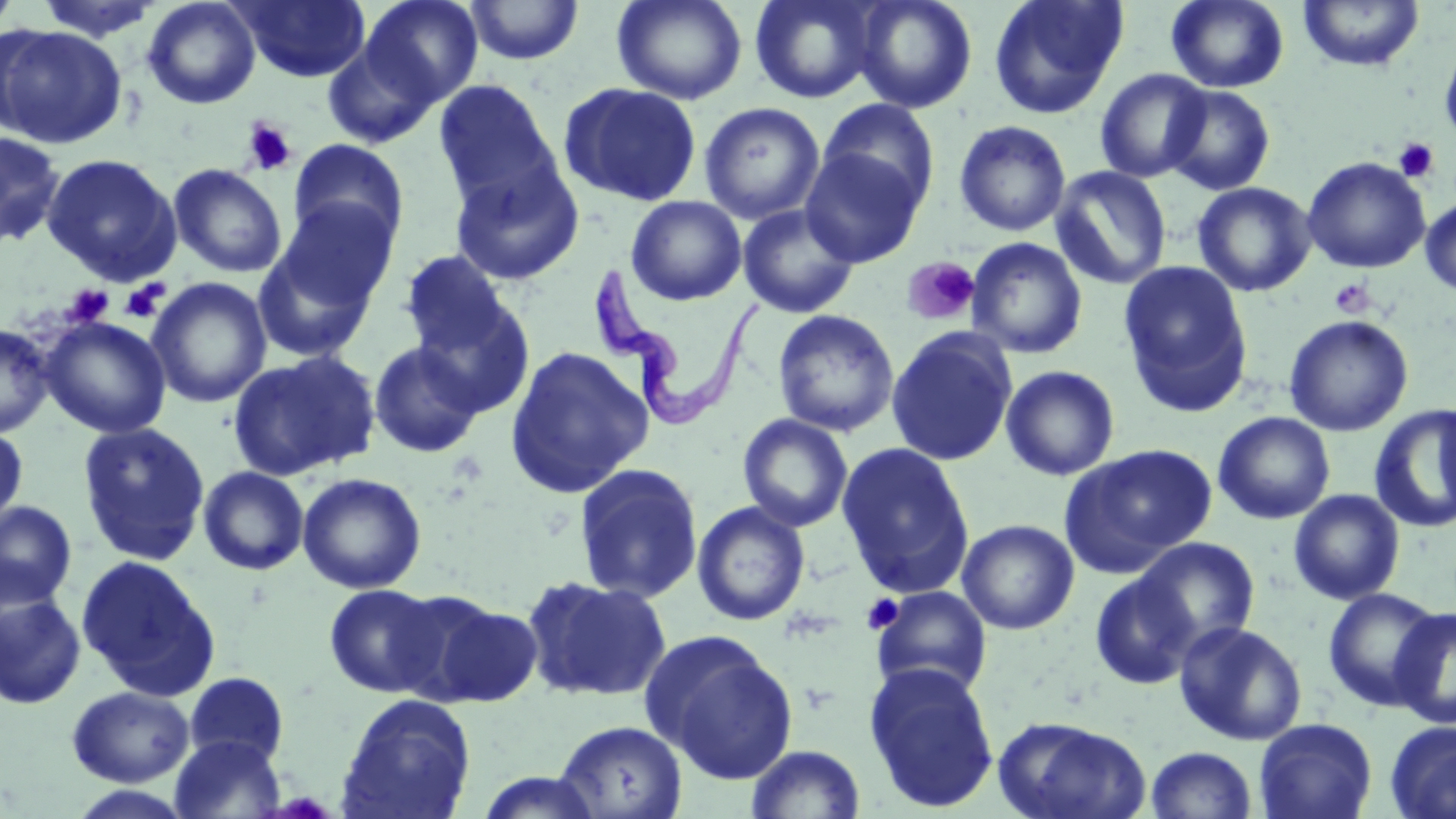 Approximate bounding boxes as (x1,y1)-(x2,y2) corner pairs in pixels. Platelet locations: (242,119)-(297,176), (1393,137)-(1438,183), (901,256)-(979,326), (1329,278)-(1376,319), (121,280)-(168,322), (65,285)-(114,327), (862,593)-(904,635). Uninfected red blood cell locations: (0,0)-(22,36), (34,0)-(166,43), (141,0)-(261,110), (235,0)-(371,83), (361,0)-(484,106), (612,0)-(748,105), (749,0)-(884,103), (852,0)-(978,113), (987,0)-(1128,120), (1166,0)-(1289,93), (1297,0)-(1425,73), (464,1)-(584,65), (0,24)-(126,148), (1439,36)-(1456,151), (322,40)-(439,148), (1095,68)-(1211,183), (432,79)-(563,211), (559,82)-(703,207), (1162,84)-(1277,196), (818,98)-(940,211), (699,102)-(825,224), (953,120)-(1071,236), (0,131)-(65,248), (287,139)-(409,252), (800,147)-(925,267), (42,153)-(181,285), (448,156)-(585,286), (1302,156)-(1431,273), (168,163)-(287,278), (1049,166)-(1172,290), (1193,181)-(1316,297), (626,195)-(747,305), (1420,195)-(1456,298), (273,198)-(399,317), (737,204)-(860,318), (252,233)-(384,364), (966,237)-(1088,360), (400,251)-(512,358), (1118,260)-(1253,416), (146,277)-(272,408), (413,297)-(536,418), (772,309)-(900,437), (1283,314)-(1414,436), (39,316)-(172,438), (0,322)-(55,438), (885,326)-(1019,466), (368,341)-(485,458), (505,346)-(654,497), (228,350)-(381,481), (1000,365)-(1121,481), (1369,405)-(1456,532), (1213,411)-(1335,525), (737,414)-(854,532), (76,422)-(211,566), (0,426)-(28,533), (836,442)-(975,599), (1061,443)-(1215,574), (573,463)-(704,604), (198,466)-(309,575), (297,472)-(427,594), (1288,489)-(1405,604), (0,500)-(77,610), (692,500)-(811,626), (957,519)-(1079,634), (1133,537)-(1260,652), (76,555)-(220,700), (1090,571)-(1199,690), (522,575)-(672,703), (323,583)-(445,698), (870,585)-(993,698), (1322,586)-(1444,712), (0,589)-(86,710), (422,598)-(546,708), (1390,606)-(1456,729), (1174,620)-(1308,745), (643,630)-(799,784), (864,662)-(1000,813), (183,671)-(291,769), (68,686)-(194,787), (336,693)-(477,818), (993,715)-(1150,819), (1253,717)-(1378,819), (554,720)-(688,819), (1385,721)-(1456,819), (169,734)-(287,818), (745,743)-(866,819), (1145,746)-(1258,819), (473,770)-(605,818), (65,785)-(196,819). Trypanosoma brucei locations: (591,261)-(761,431). Slide-level diagnosis: Trypanosoma brucei. Light microscopy. Thin blood film. May-Grünwald-Giemsa stain. Captured at 1000x magnification. One field of a larger specimen. Image is 1456×819 pixels.